Name the blood parasite species.
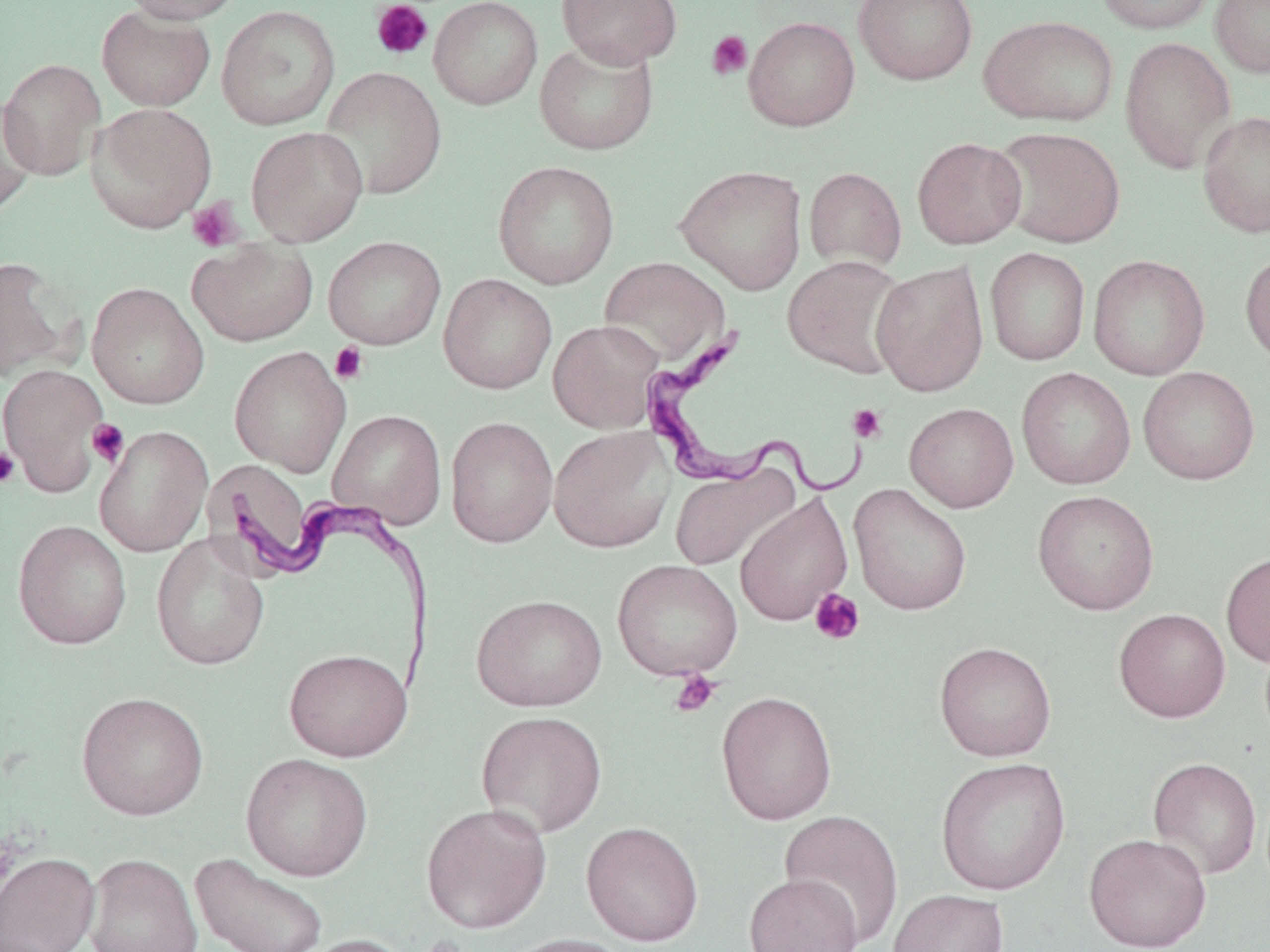
Trypanosoma brucei.

Approximate bounding boxes as (x1,y1)-(x2,y2) corner pairs in pixels. Platelet locations (subset): (371,0)-(434,61), (706,30)-(753,80), (186,199)-(244,252), (330,342)-(369,385), (848,404)-(887,443), (87,419)-(129,467), (0,447)-(20,488), (810,588)-(865,645), (669,670)-(721,717). Uninfected red blood cell locations (subset): (120,0)-(242,25), (428,0)-(543,109), (557,0)-(682,68), (853,0)-(978,85), (1094,0)-(1216,35), (1210,0)-(1270,78), (96,5)-(216,111), (216,5)-(340,130), (978,15)-(1119,126), (743,16)-(860,131), (534,37)-(659,155), (1119,37)-(1237,173), (0,58)-(107,180), (318,66)-(447,199), (0,94)-(40,218), (1197,110)-(1270,238), (246,125)-(368,246), (991,126)-(1126,249), (912,137)-(1027,249), (492,160)-(620,289), (674,164)-(807,294), (803,167)-(906,272), (323,236)-(446,349), (187,239)-(318,346), (984,247)-(1091,366), (1240,249)-(1270,366), (1088,254)-(1210,380), (0,256)-(78,382), (598,256)-(731,369), (783,256)-(910,378), (871,261)-(989,397), (438,273)-(557,395), (87,282)-(209,409), (547,319)-(666,433), (229,346)-(351,476), (0,363)-(110,495), (1138,366)-(1260,485), (1016,367)-(1136,489), (905,403)-(1019,512), (327,409)-(447,529), (445,416)-(558,548), (94,425)-(213,557), (548,425)-(676,553), (204,459)-(316,575), (669,462)-(800,572), (848,483)-(972,616), (1032,489)-(1159,615), (734,492)-(853,627), (12,519)-(132,650), (151,533)-(271,671), (1221,550)-(1270,667), (612,559)-(743,681), (471,594)-(607,712), (1113,608)-(1231,722), (934,641)-(1057,761), (283,648)-(413,761), (716,690)-(837,825), (76,691)-(209,821), (476,710)-(607,838), (240,753)-(374,881), (936,757)-(1071,895), (1147,757)-(1262,879), (421,802)-(552,933), (779,809)-(904,947), (581,821)-(703,945), (1083,832)-(1211,952), (0,851)-(100,952), (191,852)-(329,952), (83,853)-(203,952), (744,872)-(863,952), (888,889)-(1009,952), (287,933)-(413,952), (502,933)-(635,952). Trypanosoma brucei locations: (644,325)-(873,505), (221,477)-(440,700). Thin blood smear. Image is 1270×952 pixels. May-Grünwald-Giemsa stain. 1000x magnification. One field of a larger specimen. Optical microscopy.